Assess the morphology of the red blood cells.
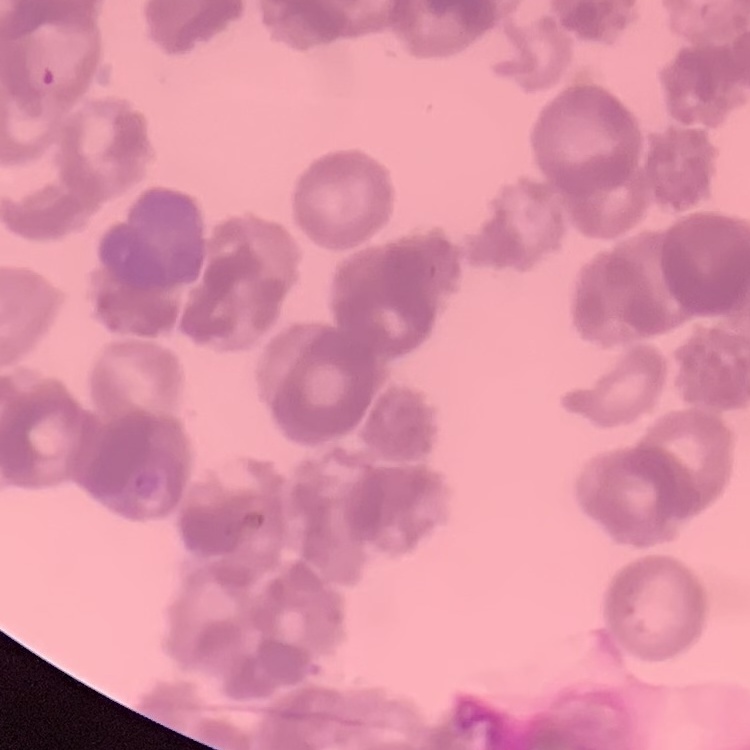

Rouleaux formation.

Thin peripheral smear. Square crop of a larger photomicrograph. Field's or Giemsa stain.